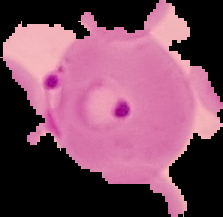

Summary:
  - Preparation: thin blood film
  - Image size: 223×217 pixels
  - Malaria status: parasitized
  - Image type: cell region segmented out of the field of view; surrounding area masked to black